Assess the morphology of the erythrocytes.
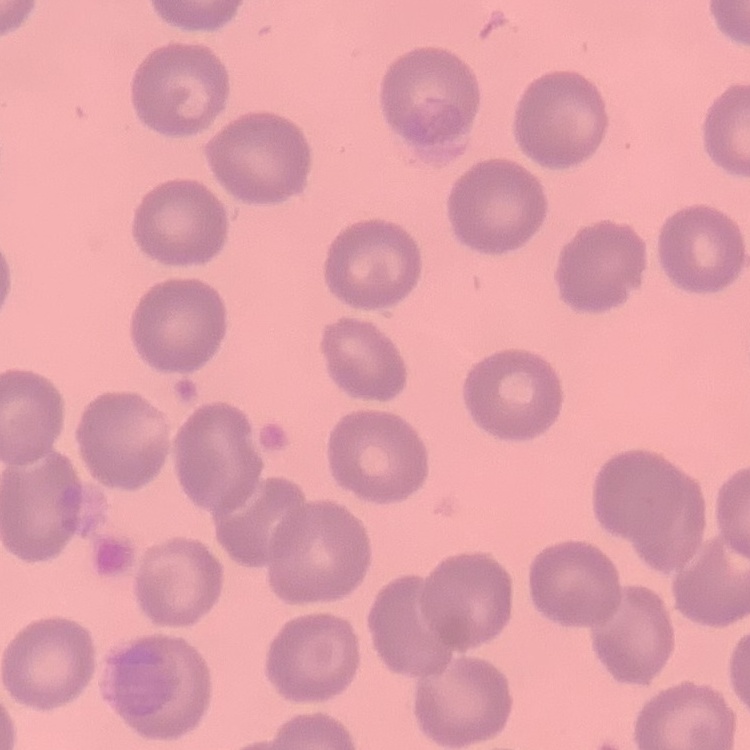
No rouleaux formation.

One tile cut from a larger photomicrograph. Thin peripheral smear. Field's or Giemsa stain.